Locate every blood parasite and identify its species.
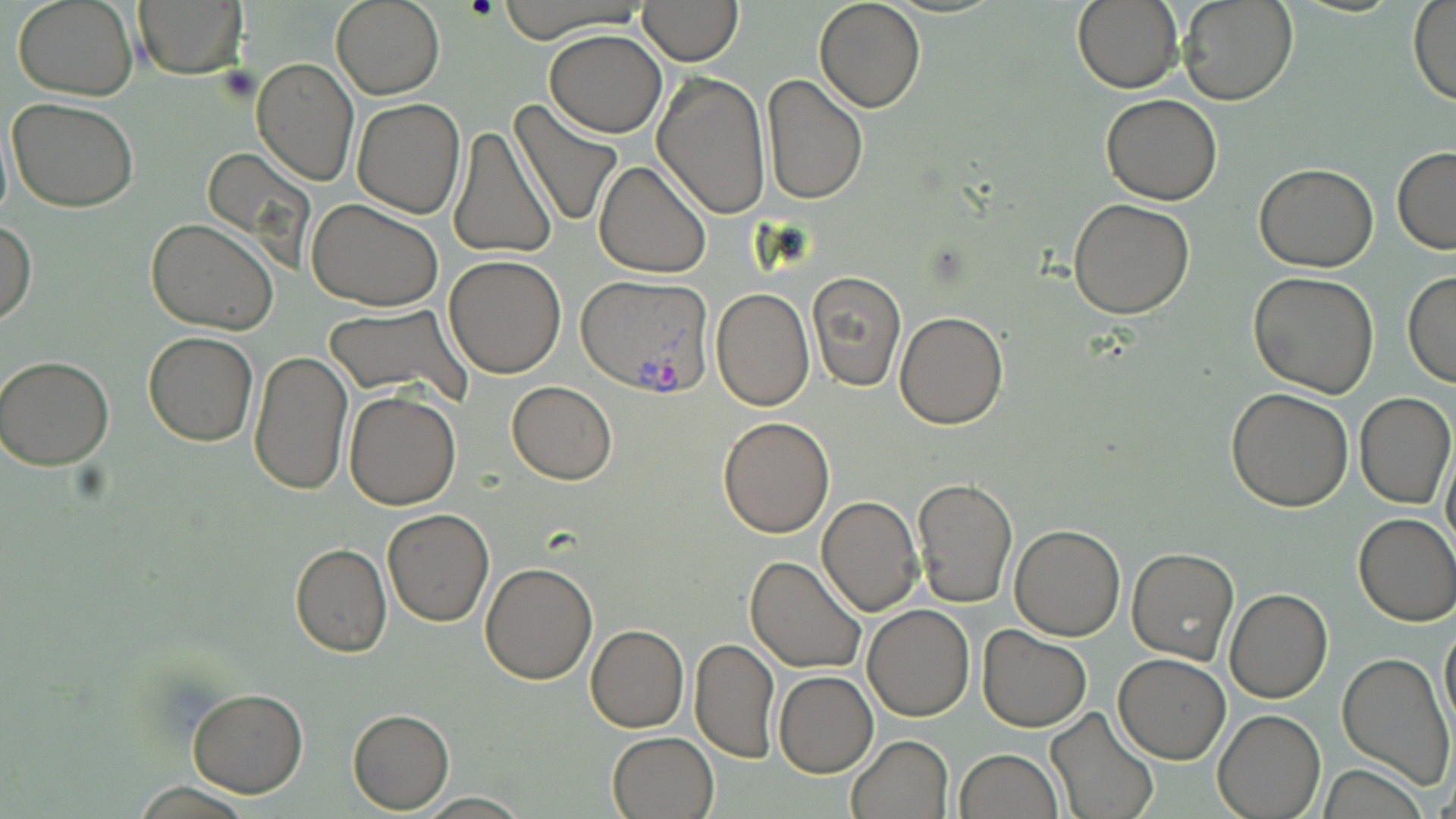

Approximate bounding boxes as named x1/y1/x2/y2 corners in pixels.
Plasmodium vivax-infected red blood cells: (x1=576, y1=273, x2=715, y2=394).
No Plasmodium falciparum, Plasmodium ovale, Plasmodium malariae, Babesia divergens, or Trypanosoma brucei observed.

{
  "slide_level_diagnosis": "Plasmodium vivax",
  "stain": "May-Grünwald-Giemsa",
  "preparation": "thin blood film",
  "magnification": "1000x",
  "uninfected_red_blood_cell_locations": "approximate bounding boxes as named x1/y1/x2/y2 corners in pixels: (x1=14, y1=0, x2=138, y2=101), (x1=133, y1=0, x2=245, y2=78), (x1=331, y1=0, x2=444, y2=99), (x1=494, y1=0, x2=650, y2=39), (x1=813, y1=0, x2=926, y2=112), (x1=1070, y1=0, x2=1185, y2=92), (x1=1177, y1=0, x2=1298, y2=106), (x1=1407, y1=0, x2=1456, y2=105), (x1=638, y1=1, x2=742, y2=64), (x1=544, y1=30, x2=666, y2=137), (x1=252, y1=58, x2=358, y2=186), (x1=652, y1=71, x2=773, y2=220), (x1=761, y1=74, x2=868, y2=207), (x1=1099, y1=94, x2=1222, y2=205), (x1=6, y1=97, x2=139, y2=211), (x1=352, y1=98, x2=466, y2=219), (x1=509, y1=99, x2=625, y2=228), (x1=446, y1=124, x2=556, y2=262), (x1=1394, y1=147, x2=1456, y2=253), (x1=206, y1=148, x2=316, y2=285), (x1=592, y1=160, x2=711, y2=279), (x1=1254, y1=162, x2=1379, y2=272), (x1=1068, y1=198, x2=1196, y2=319), (x1=307, y1=200, x2=442, y2=311), (x1=0, y1=216, x2=36, y2=327), (x1=146, y1=220, x2=279, y2=335), (x1=443, y1=254, x2=567, y2=377), (x1=1248, y1=270, x2=1380, y2=397), (x1=807, y1=271, x2=906, y2=391), (x1=1404, y1=271, x2=1456, y2=388), (x1=711, y1=287, x2=815, y2=411), (x1=322, y1=303, x2=471, y2=404), (x1=895, y1=311, x2=1008, y2=428), (x1=143, y1=330, x2=259, y2=447), (x1=249, y1=350, x2=352, y2=494), (x1=1, y1=355, x2=117, y2=471), (x1=507, y1=380, x2=617, y2=484), (x1=1225, y1=387, x2=1353, y2=512), (x1=345, y1=389, x2=461, y2=510), (x1=1355, y1=393, x2=1455, y2=509), (x1=716, y1=415, x2=835, y2=538), (x1=1441, y1=438, x2=1456, y2=562), (x1=913, y1=477, x2=1020, y2=610), (x1=816, y1=495, x2=923, y2=617), (x1=384, y1=509, x2=494, y2=627), (x1=1354, y1=513, x2=1456, y2=627), (x1=1010, y1=525, x2=1126, y2=640), (x1=290, y1=542, x2=390, y2=657), (x1=1126, y1=547, x2=1240, y2=664), (x1=747, y1=555, x2=868, y2=674), (x1=480, y1=560, x2=598, y2=684), (x1=1225, y1=588, x2=1332, y2=703), (x1=862, y1=603, x2=976, y2=720), (x1=1439, y1=617, x2=1455, y2=742), (x1=587, y1=624, x2=690, y2=732), (x1=976, y1=625, x2=1093, y2=731), (x1=690, y1=638, x2=779, y2=762), (x1=1114, y1=652, x2=1232, y2=763), (x1=1336, y1=652, x2=1453, y2=788), (x1=774, y1=672, x2=878, y2=777), (x1=188, y1=688, x2=308, y2=798), (x1=1045, y1=706, x2=1159, y2=819), (x1=1213, y1=708, x2=1326, y2=819), (x1=349, y1=709, x2=454, y2=812), (x1=607, y1=730, x2=720, y2=819), (x1=846, y1=734, x2=953, y2=819), (x1=954, y1=749, x2=1063, y2=818), (x1=1314, y1=766, x2=1427, y2=819)",
  "modality": "optical microscopy",
  "field_of_view": "single",
  "image_size": "1456×819 pixels"
}